Locate every leukocyte (white blood cell).
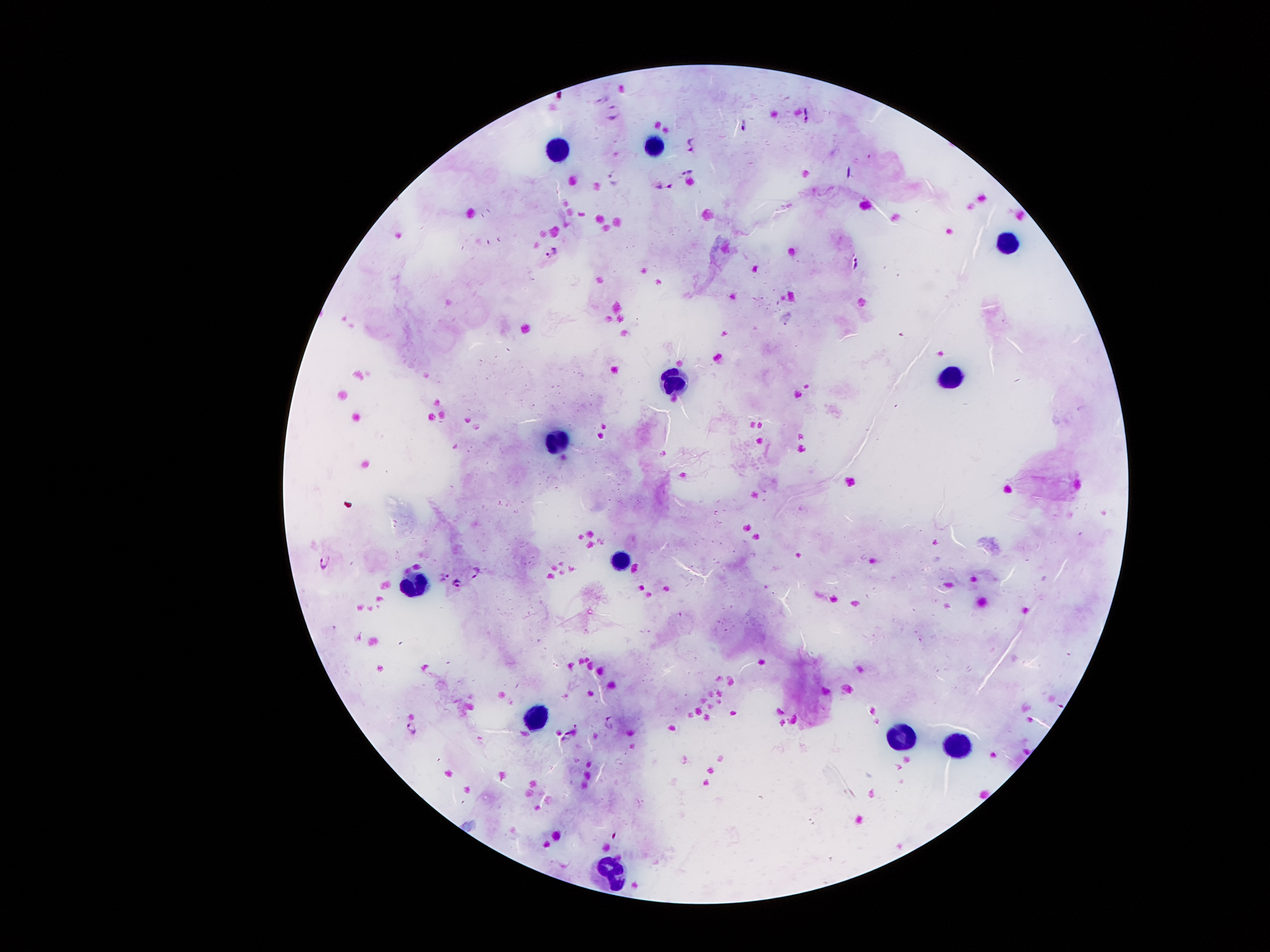
Approximate centers as {x, y} in pixels.
Leukocytes: {655, 146}, {560, 149}, {1003, 236}, {946, 375}, {672, 382}, {556, 442}, {618, 562}, {412, 584}, {538, 714}, {900, 735}, {955, 745}, {616, 871}.

Summary:
  - Plasmodium parasite locations: {611, 112}, {805, 115}, {691, 144}, {688, 171}, {614, 176}, {661, 186}, {552, 252}, {856, 263}, {324, 562}, {478, 571}, {443, 577}, {455, 585}, {610, 723}, {414, 728}, {565, 739}
  - Field of view: one from this slide
  - Magnification: 100x
  - Stain: Giemsa
  - Capture: smartphone through the microscope eyepiece
  - Image size: 1270×952 pixels
  - Patient malaria status: positive for Plasmodium falciparum
  - Preparation: thick blood film